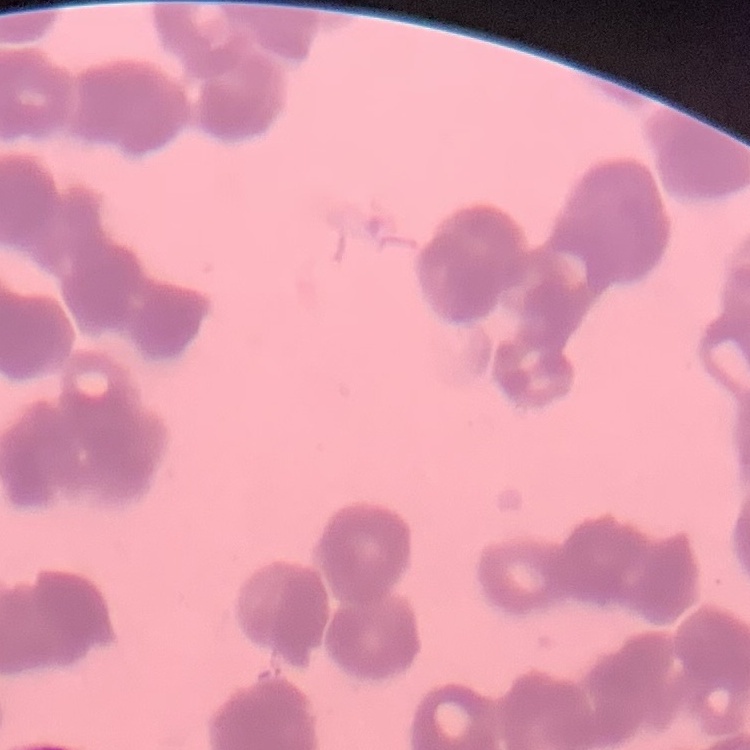

The red blood cells exhibit rouleaux formation. One tile cut from a larger photomicrograph. Stained with either Field's or Giemsa. Thin peripheral smear.